Identify the preparation type.
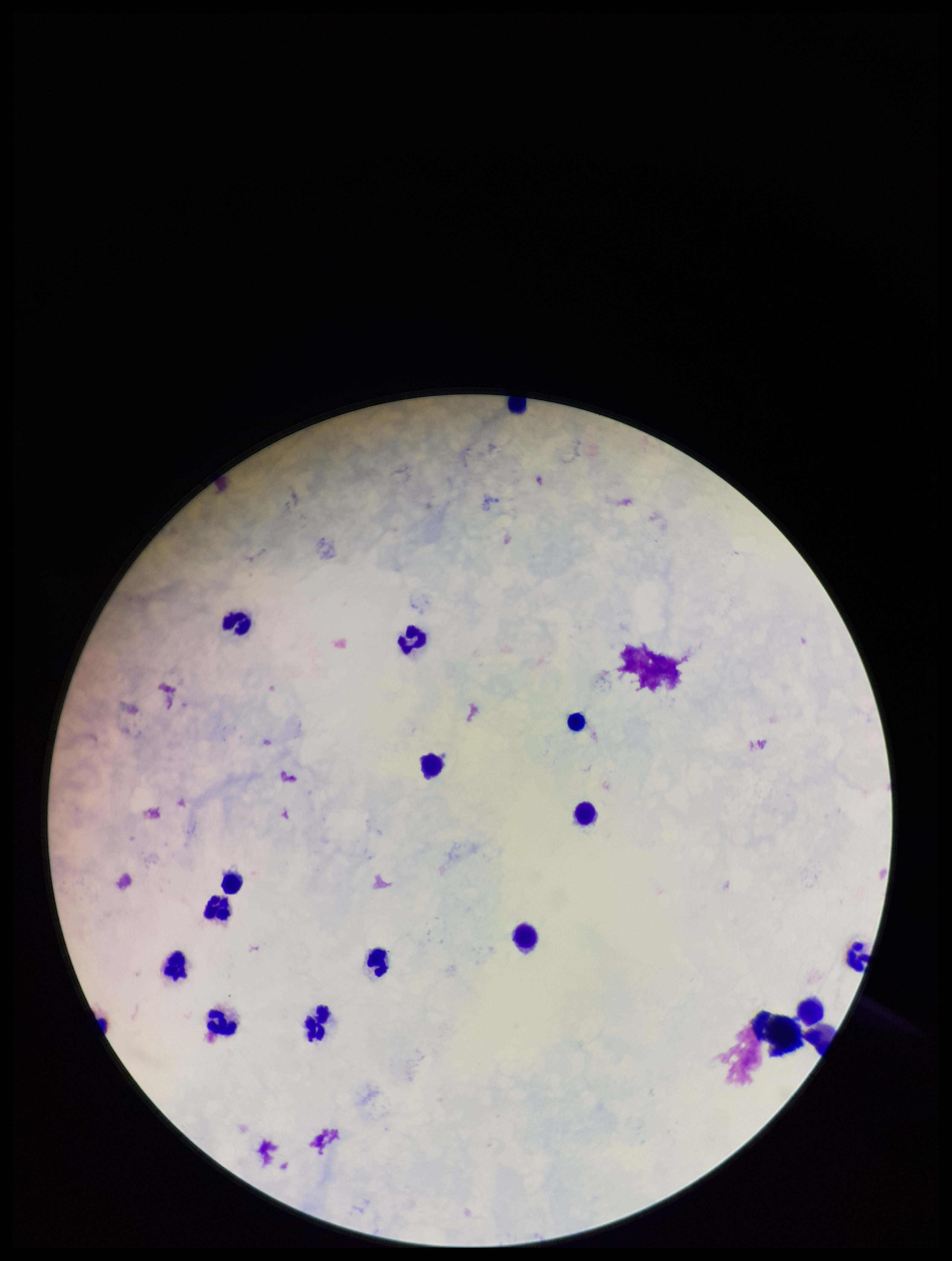
Thick.

{
  "image_size": "952×1261 pixels",
  "plasmodium_parasites": "none seen",
  "patient_malaria_status": "negative",
  "stain": "Giemsa",
  "parasite_count": 0,
  "field_of_view": "one from this slide",
  "capture": "smartphone photograph through the microscope eyepiece",
  "leukocyte_count": 16
}